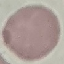

malaria_status: uninfected
preparation: thin smear
stain: Giemsa
image_type: automatically extracted cell patch, resized to 64 × 64 pixels
capture: smartphone camera at the microscope eyepiece